Classify this cell by malaria status.
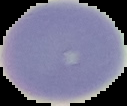

Uninfected.

preparation = thin blood film
image type = segmented cell region on a black background
image size = 127×106 pixels